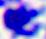
identification = white blood cell
modality = photomicrograph
magnification = 400x